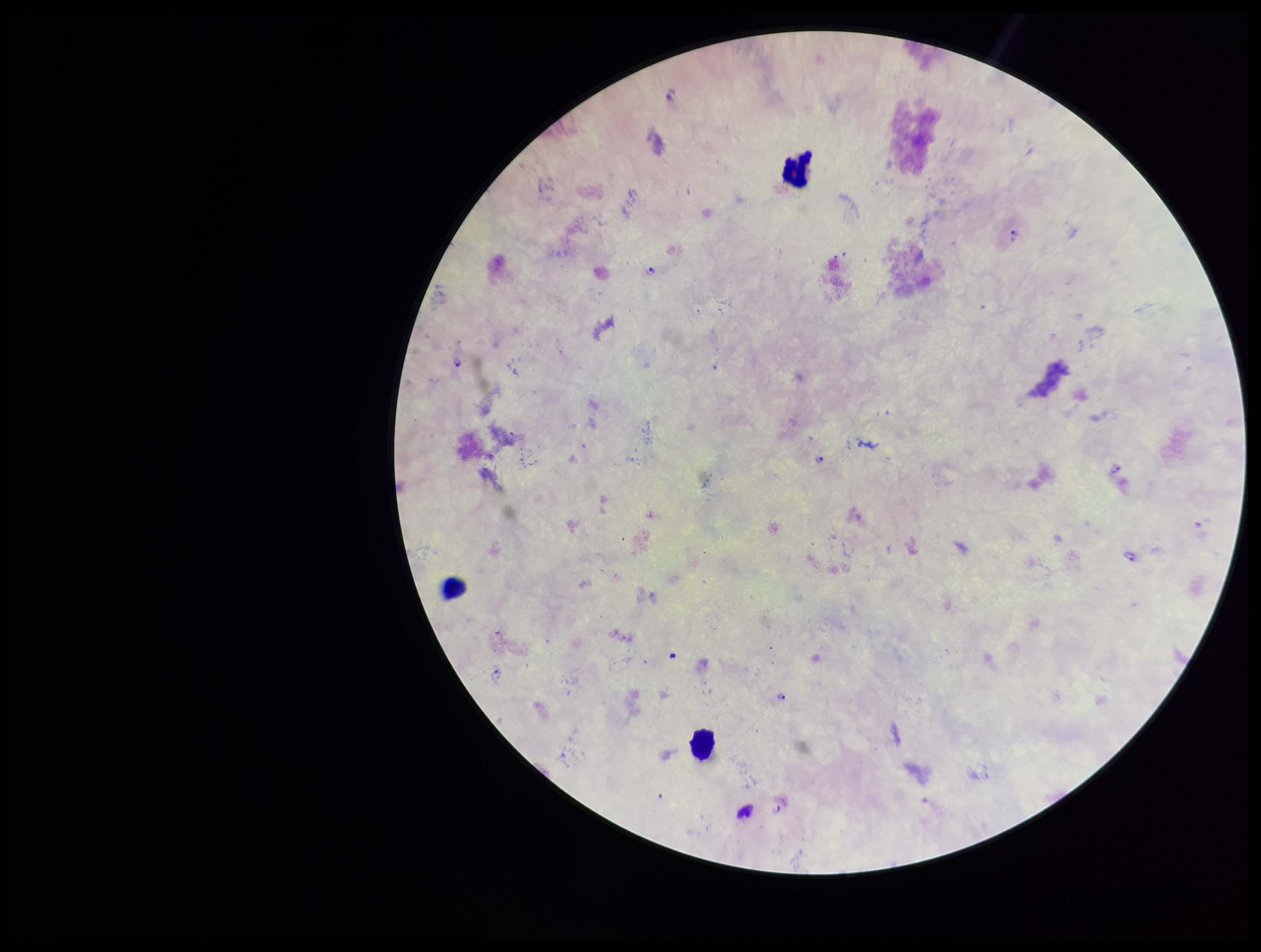
{
  "preparation": "thick smear",
  "stain": "Giemsa",
  "patient_malaria_status": "positive",
  "leukocyte_count": 3,
  "species_reported_for_this_patient": "Plasmodium falciparum",
  "parasite_count": 7,
  "field_of_view": "one from this slide",
  "plasmodium_parasites": "seen",
  "capture": "smartphone photograph through the microscope eyepiece",
  "image_size": "1261×952 pixels"
}